Identify the parasite.
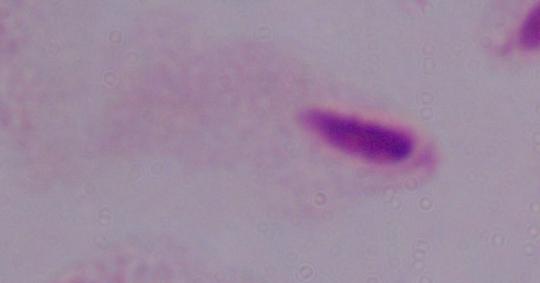

This is a trichomonad.

1000x magnification. Photomicrograph.